Classify this cell by malaria status.
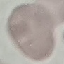

It is uninfected.

Summary:
  - Stain: Giemsa
  - Image type: cell patch, automatically extracted from a larger field of view and resized to 64 × 64 pixels
  - Capture: smartphone camera at the microscope eyepiece
  - Preparation: thin blood film